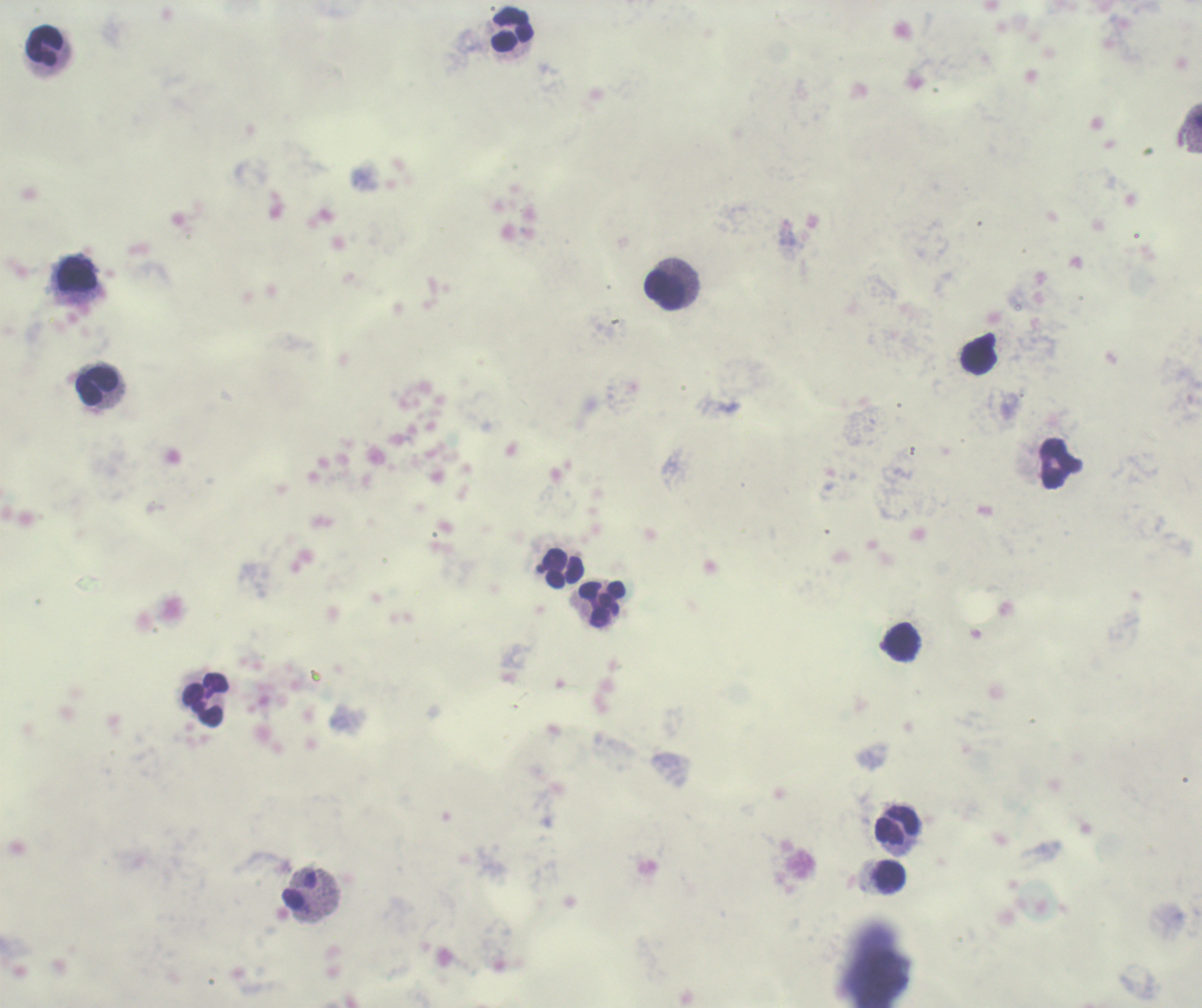

Approximate object centers, in pixels from the top-left corner.
Summary:
  - Leukocyte locations: (x=514, y=29), (x=44, y=45), (x=77, y=273), (x=665, y=290), (x=979, y=358), (x=97, y=385), (x=1060, y=463), (x=562, y=568), (x=602, y=604), (x=903, y=642), (x=206, y=699), (x=897, y=824), (x=890, y=876), (x=299, y=890)
  - Image size: 1202×1008 pixels
  - Result: no malaria parasites detected
  - Magnification: 100x
  - Context: previously used in a real diagnosis
  - Background quality: unsatisfactory
  - Field of view: single
  - Preparation: thick blood smear
  - Stain: Romanowsky
  - Coloration quality: bad